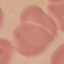
result = no malaria parasites seen
capture = smartphone through the microscope eyepiece
stain = Giemsa
preparation = thin blood smear
image type = cell patch, automatically extracted from a larger field of view and resized to 64 × 64 pixels